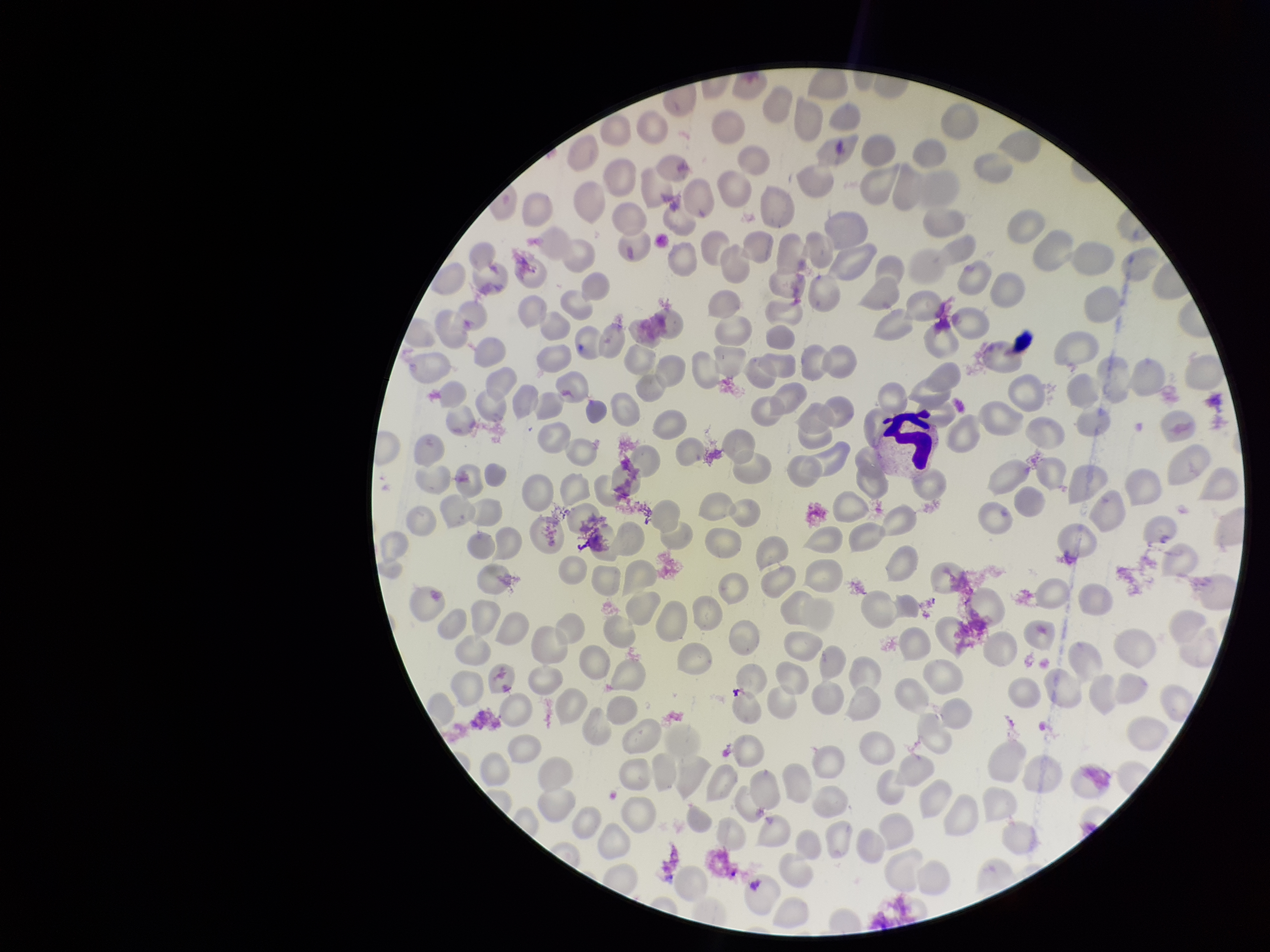

red blood cell count = 264
capture = smartphone photograph through the microscope eyepiece
image size = 1270×952 pixels
species reported for this patient = Plasmodium vivax
parasitized red blood cells = none detected
field of view = one from this slide
patient malaria status = infected
parasitized red blood cell count = 0
stain = Giemsa
preparation = thin blood smear